Assess this cell for malaria.
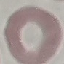
It is uninfected.

stain = Giemsa
capture = smartphone camera at the microscope eyepiece
preparation = thin blood smear
image type = automatically extracted cell patch, resized to 64 × 64 pixels